Point out each Plasmodium parasite.
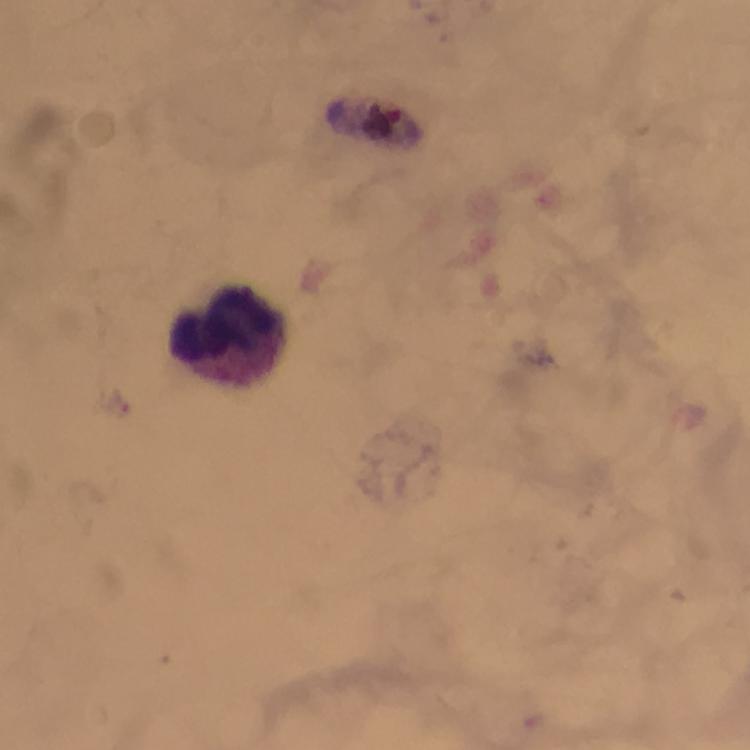
No Plasmodium parasites seen.

Approximate object centers, in pixels from the top-left corner. Leukocyte locations: (x=229, y=332). Thick blood smear. 100x magnification. Giemsa-stained preparation. Immersion oil applied. Cropped region of a single field of view. Image is 750×750 pixels. From a diagnostic examination for malaria. Smartphone photograph taken through a microscope.